Report the malaria status of this cell.
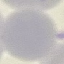
Uninfected.

capture = smartphone camera at the microscope eyepiece
image type = cell patch, automatically extracted from a larger field of view and resized to 64 × 64 pixels
stain = Giemsa
preparation = thin smear